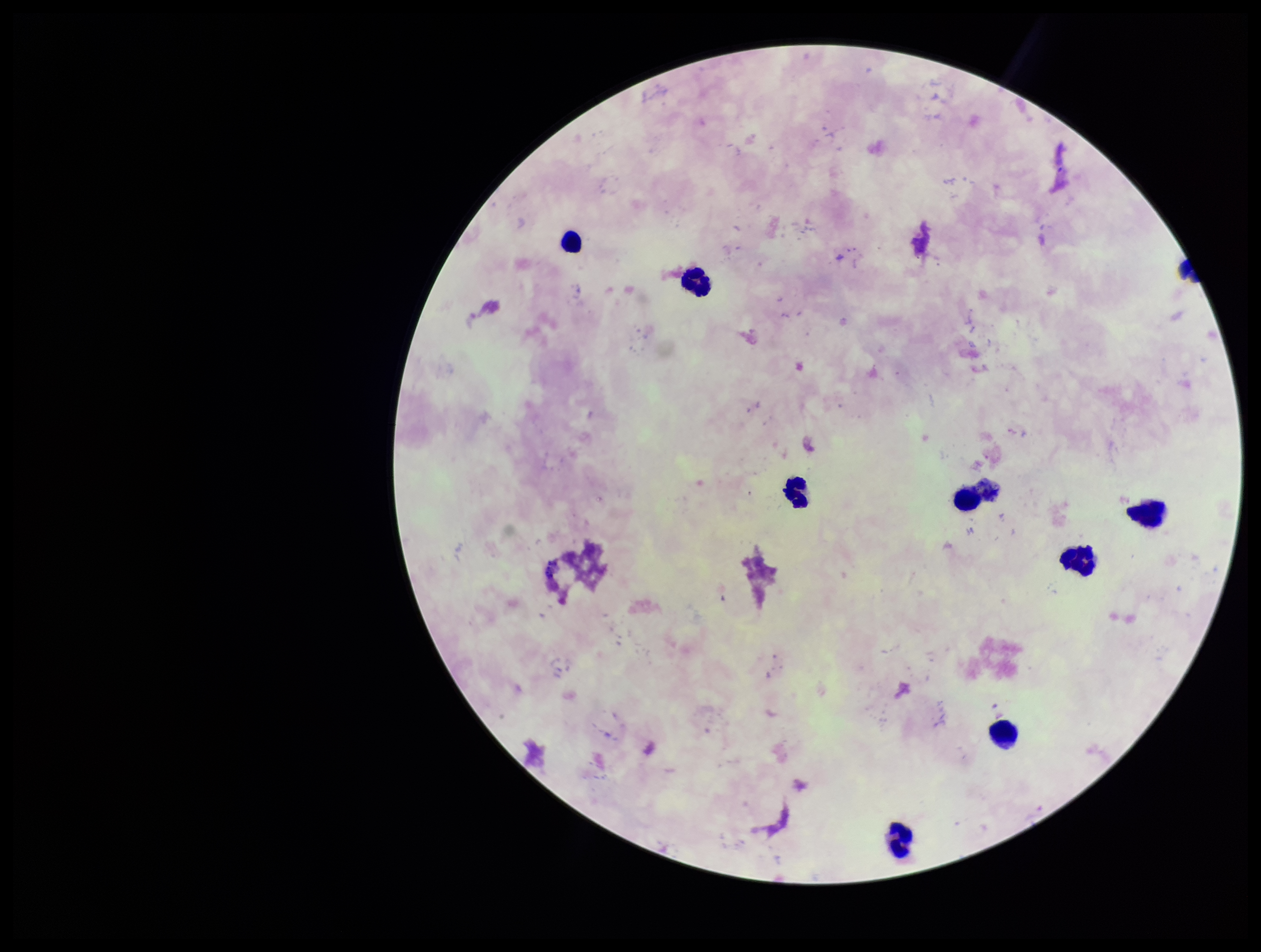

Summary:
  - Preparation: thick smear
  - Patient malaria status: negative
  - Plasmodium parasites: none identified
  - Image size: 1261×952 pixels
  - Stain: Giemsa
  - Capture: smartphone photograph through the microscope eyepiece
  - Leukocyte count: 9
  - Parasite count: 0
  - Field of view: single